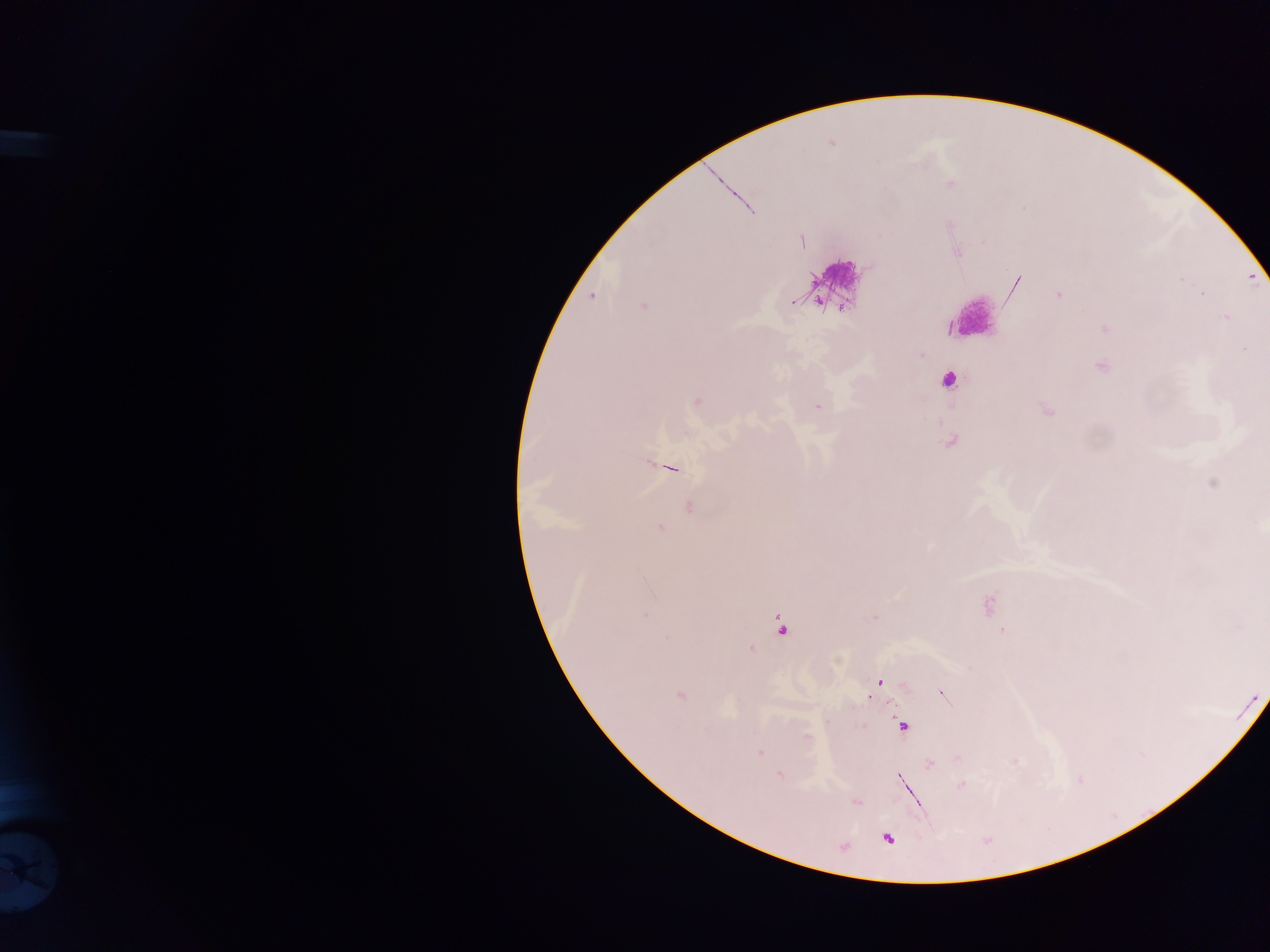
Approximate centers as (x, y) in pixels. Malaria parasite locations: (950, 183), (802, 240), (957, 253), (1058, 295), (592, 296), (643, 305), (1225, 317), (1105, 329), (1101, 367), (948, 381), (696, 402), (818, 406), (670, 468), (688, 507), (660, 529), (645, 617), (780, 625), (1003, 630), (667, 637), (751, 649), (879, 683), (942, 695), (680, 696), (903, 726), (806, 736), (759, 753), (929, 764), (780, 775), (899, 779), (961, 784), (856, 802), (887, 838). Leukocyte locations: (836, 274), (981, 317). Thick blood film. Collected in Ghana. Single field of view. Image is 1270×952 pixels. Mobile-phone photograph taken through the microscope.